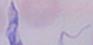
identification: trypanosome
modality: photomicrograph
magnification: 1000x